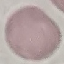

{
  "malaria_status": "uninfected",
  "stain": "Giemsa",
  "capture": "smartphone camera at the microscope eyepiece",
  "preparation": "thin smear",
  "image_type": "automatically extracted cell patch, resized to 64 × 64 pixels"
}